Name the parasite shown.
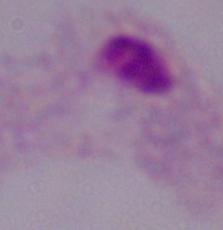
A trichomonad.

Summary:
  - Modality: micrograph
  - Magnification: 1000x